Assess this cell for malaria.
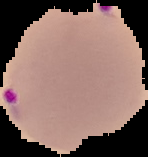
Parasitized.

Image is 148×157 pixels. Cell region segmented out of the field of view; the surrounding area is masked to black. From a thin blood film.